Assess this cell for malaria.
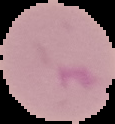
It is parasitized.

Image is 115×124 pixels. Cell region segmented out of the field of view; the surrounding area is masked to black. From a thin blood smear.